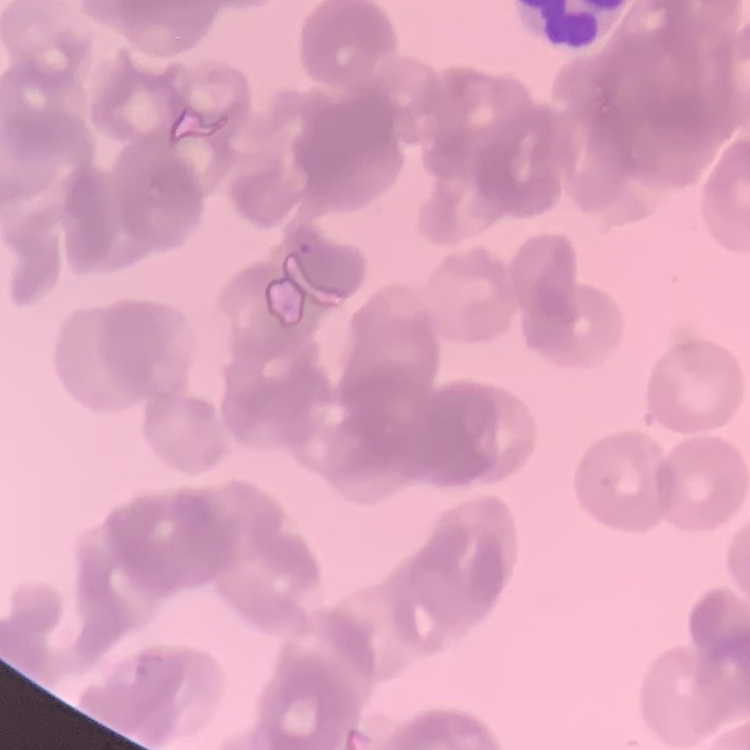

red blood cell morphology = rouleaux formation
image type = one tile cut from a larger photomicrograph
stain = Field's or Giemsa
preparation = thin peripheral smear